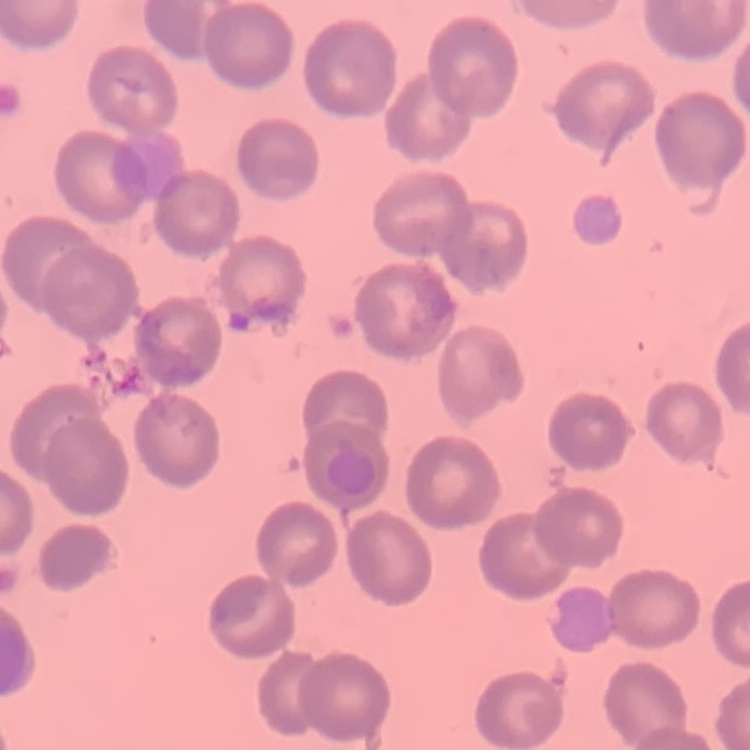

erythrocyte_morphology: no rouleaux formation
image_type: square crop of a larger photomicrograph
preparation: thin blood smear
stain: Field's or Giemsa